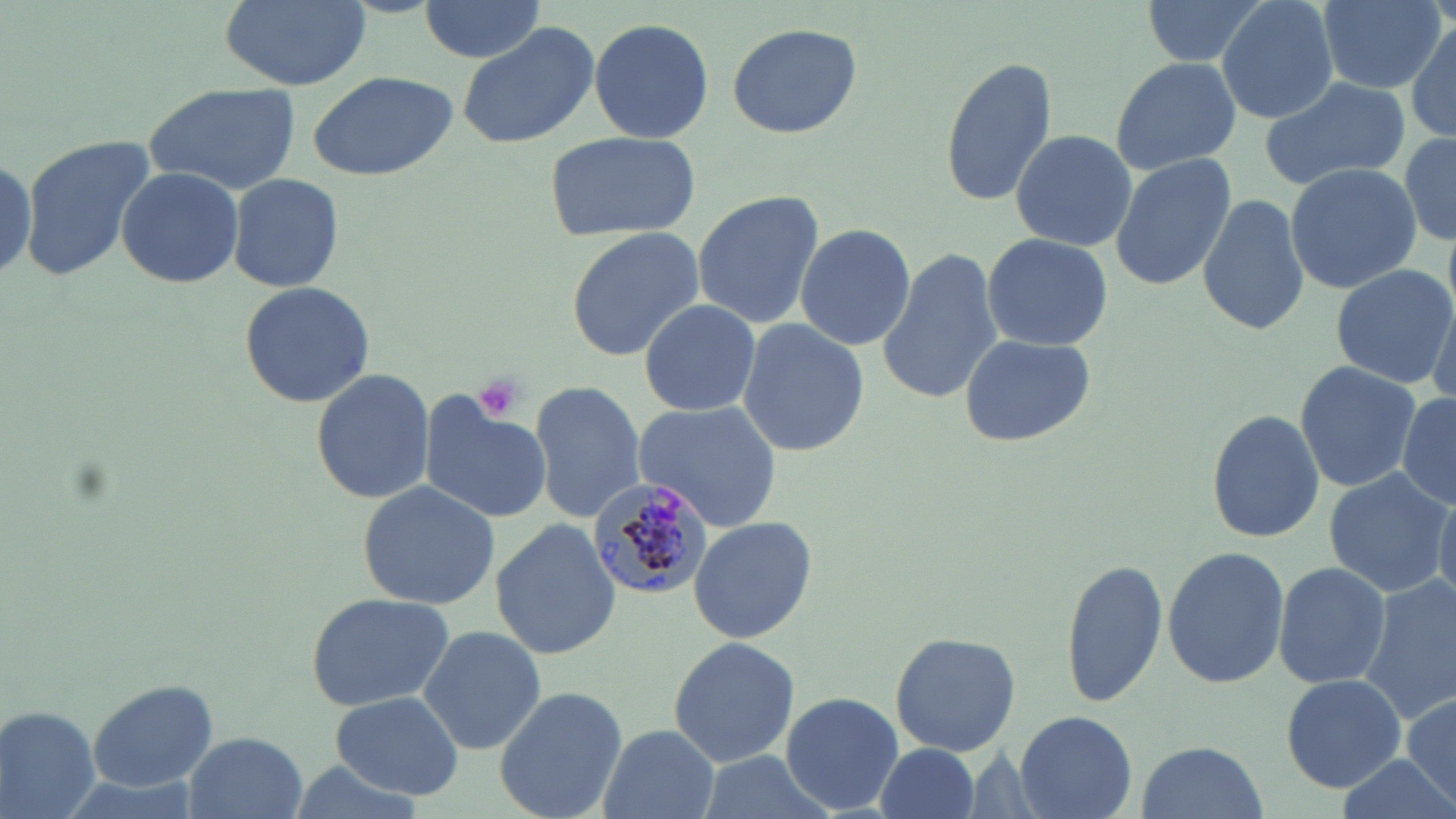 Approximate bounding boxes as [x1, y1, x2, y2] in pixels. Platelet locations: [469, 372, 531, 422]. Uninfected red blood cell locations: [219, 0, 374, 91], [1144, 0, 1278, 72], [1216, 0, 1340, 124], [417, 1, 546, 66], [1317, 1, 1445, 93], [587, 18, 714, 143], [1408, 20, 1456, 145], [457, 22, 597, 151], [726, 22, 863, 138], [937, 53, 1059, 207], [1108, 56, 1240, 174], [305, 68, 460, 182], [1259, 75, 1410, 193], [141, 84, 299, 197], [544, 128, 699, 241], [1010, 130, 1135, 250], [1400, 131, 1456, 245], [19, 134, 157, 285], [1108, 153, 1237, 291], [1284, 162, 1422, 293], [114, 166, 242, 287], [227, 172, 345, 293], [692, 191, 824, 328], [1198, 191, 1310, 335], [795, 222, 915, 352], [564, 227, 704, 361], [981, 231, 1113, 352], [876, 246, 1002, 403], [1329, 262, 1454, 389], [237, 280, 376, 410], [1426, 284, 1456, 418], [638, 298, 761, 420], [736, 317, 869, 458], [956, 332, 1096, 449], [1292, 359, 1422, 495], [309, 367, 435, 505], [528, 378, 647, 522], [1396, 393, 1456, 508], [417, 395, 550, 523], [634, 400, 780, 533], [1204, 409, 1324, 544], [1321, 467, 1450, 597], [355, 481, 501, 612], [1433, 487, 1456, 607], [688, 516, 818, 647], [491, 519, 622, 659], [1161, 545, 1290, 690], [1061, 557, 1170, 710], [1273, 561, 1391, 688], [1358, 578, 1456, 721], [304, 589, 454, 712], [416, 624, 547, 757], [888, 631, 1022, 756], [667, 634, 800, 767], [1279, 673, 1406, 792], [86, 679, 217, 793], [493, 683, 627, 819], [331, 691, 465, 801], [781, 692, 905, 814], [1402, 694, 1456, 808], [1, 705, 102, 819], [1016, 710, 1137, 817], [596, 724, 720, 819], [186, 730, 306, 817], [869, 741, 987, 819], [1133, 741, 1271, 818], [696, 751, 836, 819], [1334, 756, 1453, 817], [280, 760, 428, 815]. Plasmodium malariae-infected red blood cell locations: [586, 477, 715, 597]. Slide-level diagnosis: Plasmodium malariae. Image is 1456×819 pixels. May-Grünwald-Giemsa-stained preparation. Optical microscopy. Single field of view. Thin blood film. 1000x magnification.